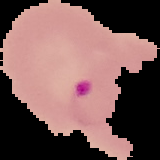

Summary:
  - Result: malaria parasites identified
  - Image size: 160×160 pixels
  - Image type: segmented cell region on a black background
  - Preparation: thin blood smear